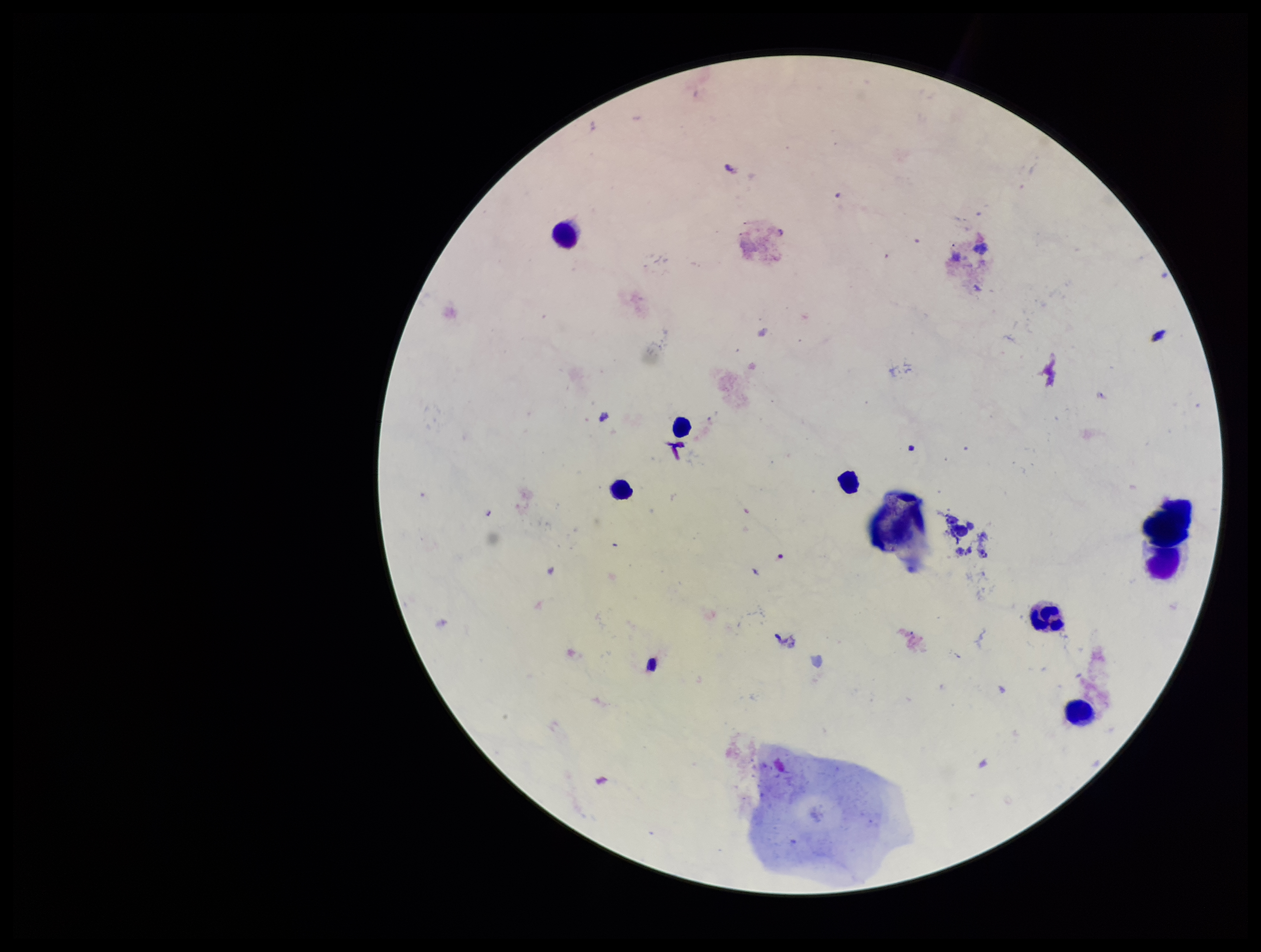
Summary:
  - Preparation: thick smear
  - Leukocyte count: 7
  - Patient malaria status: negative
  - Field of view: single
  - Plasmodium parasites: none identified
  - Image size: 1261×952 pixels
  - Parasite count: 0
  - Capture: smartphone photograph through the microscope eyepiece
  - Stain: Giemsa